Identify the parasite.
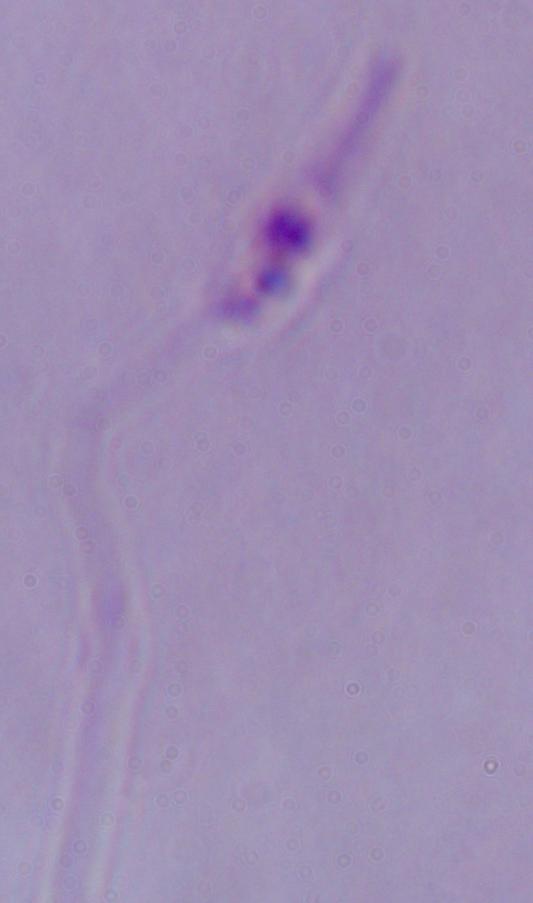

This is Leishmania.

Summary:
  - Magnification: 1000x
  - Modality: micrograph